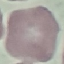

Summary:
  - Result: no malaria parasites detected
  - Capture: smartphone camera at the microscope eyepiece
  - Stain: Giemsa
  - Image type: cell patch, automatically extracted from a larger field of view and resized to 64 × 64 pixels
  - Preparation: thin blood smear